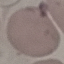
malaria_status: uninfected
stain: Giemsa
capture: smartphone through the microscope eyepiece
preparation: thin blood smear
image_type: cell patch, automatically extracted from a larger field of view and resized to 64 × 64 pixels